Identify the cell.
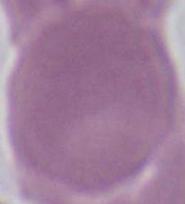
This is an erythrocyte.

1000x magnification. Photomicrograph.